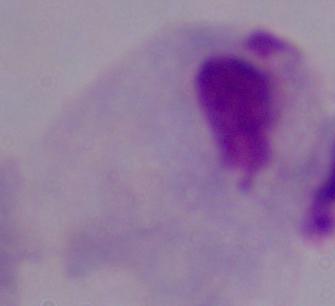
Summary:
  - Modality: micrograph
  - Magnification: 1000x
  - Identification: trichomonad